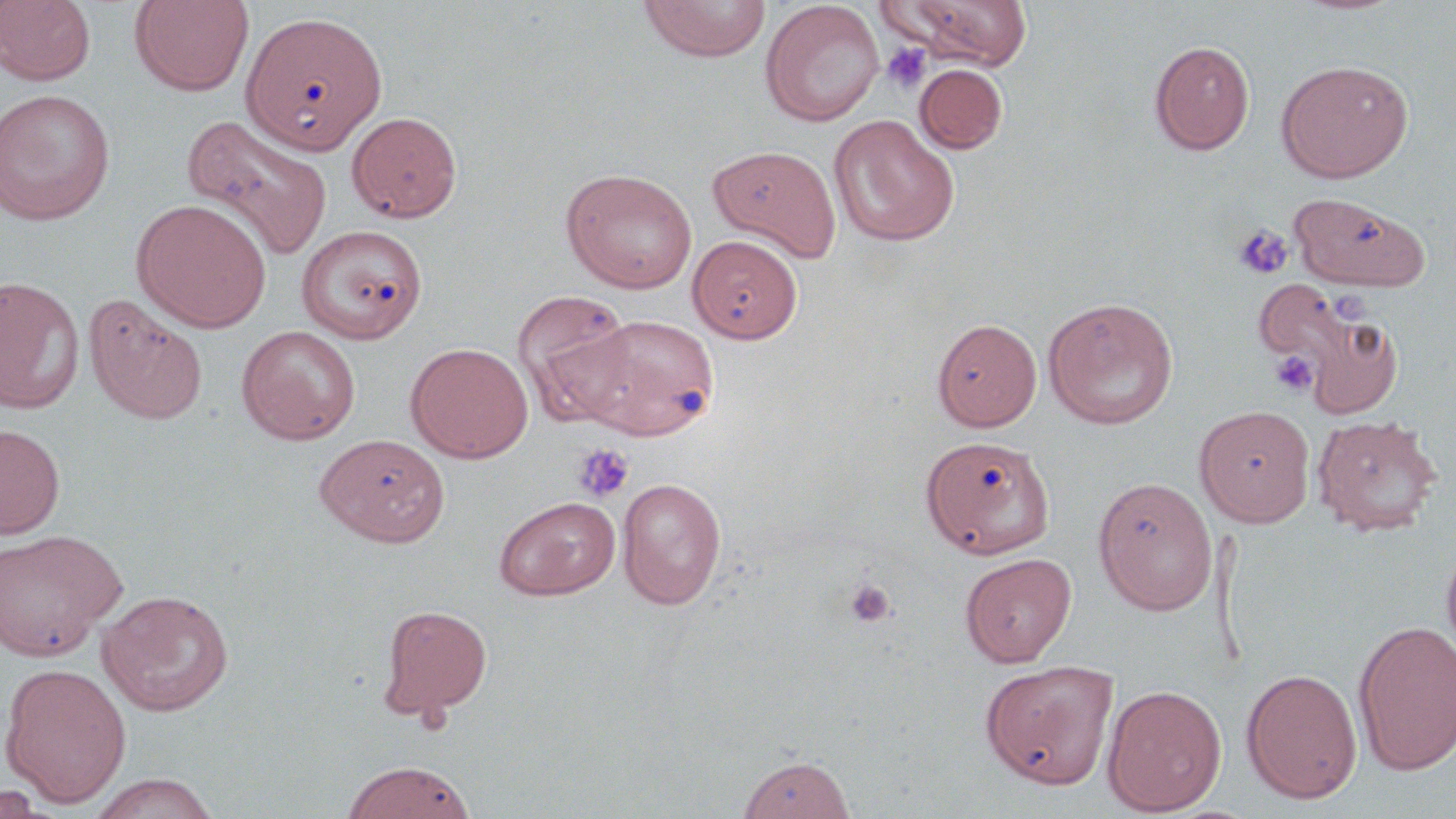
Summary:
  - Coordinate format: approximate bounding boxes as (x1, y1, x2, y2) in pixels
  - Platelet locations: (882, 43, 932, 94), (1232, 224, 1293, 280), (1330, 290, 1369, 323), (1270, 350, 1319, 397), (573, 443, 634, 503), (844, 578, 896, 627)
  - Uninfected red blood cell locations: (1, 0, 96, 86), (129, 0, 254, 96), (639, 0, 771, 62), (883, 0, 1034, 70), (760, 1, 884, 127), (242, 10, 387, 153), (1149, 40, 1254, 155), (1277, 60, 1413, 182), (915, 64, 1007, 154), (0, 89, 116, 226), (347, 110, 462, 223), (182, 114, 332, 263), (828, 114, 960, 247), (707, 144, 842, 260), (561, 167, 698, 294), (1288, 193, 1429, 292), (131, 198, 272, 333), (297, 225, 428, 344), (688, 234, 802, 343), (0, 277, 84, 414), (1256, 279, 1372, 391), (512, 290, 637, 421), (84, 294, 209, 425), (1042, 296, 1179, 430), (1291, 305, 1406, 419), (572, 313, 719, 440), (932, 318, 1042, 431), (236, 325, 361, 445), (406, 342, 533, 463), (1194, 405, 1315, 527), (1312, 415, 1442, 537), (0, 424, 65, 539), (315, 434, 449, 546), (921, 435, 1055, 559), (1093, 476, 1217, 615), (617, 477, 727, 610), (493, 496, 621, 601), (0, 529, 126, 663), (1440, 537, 1456, 665), (960, 552, 1077, 667), (96, 589, 234, 716), (377, 603, 492, 720), (1353, 620, 1456, 775), (979, 658, 1120, 789), (0, 663, 131, 806), (1241, 668, 1362, 804), (1102, 683, 1227, 816), (736, 755, 856, 818), (340, 760, 477, 819), (84, 772, 221, 819), (0, 784, 54, 819)
  - Slide-level diagnosis: negative for blood parasites
  - Modality: light microscopy
  - Image size: 1456×819 pixels
  - Stain: May-Grünwald-Giemsa
  - Preparation: thin blood film
  - Field of view: single
  - Magnification: 1000x